Report the malaria status of this cell.
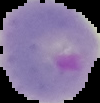

It is parasitized.

preparation = thin blood smear
image type = segmented cell region with the area outside set to black
image size = 100×103 pixels